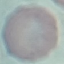 Malaria status: uninfected. Giemsa stain. Acquired by smartphone through the microscope eyepiece. Thin blood smear. Automatically extracted cell patch, resized to 64 × 64 pixels.